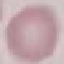
Summary:
  - Malaria status: uninfected
  - Stain: Giemsa
  - Capture: smartphone through the microscope eyepiece
  - Image type: automatically extracted cell patch, resized to 64 × 64 pixels
  - Preparation: thin smear